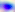

magnification = 400x
modality = micrograph
identification = Toxoplasma gondii